Outline each white blood cell.
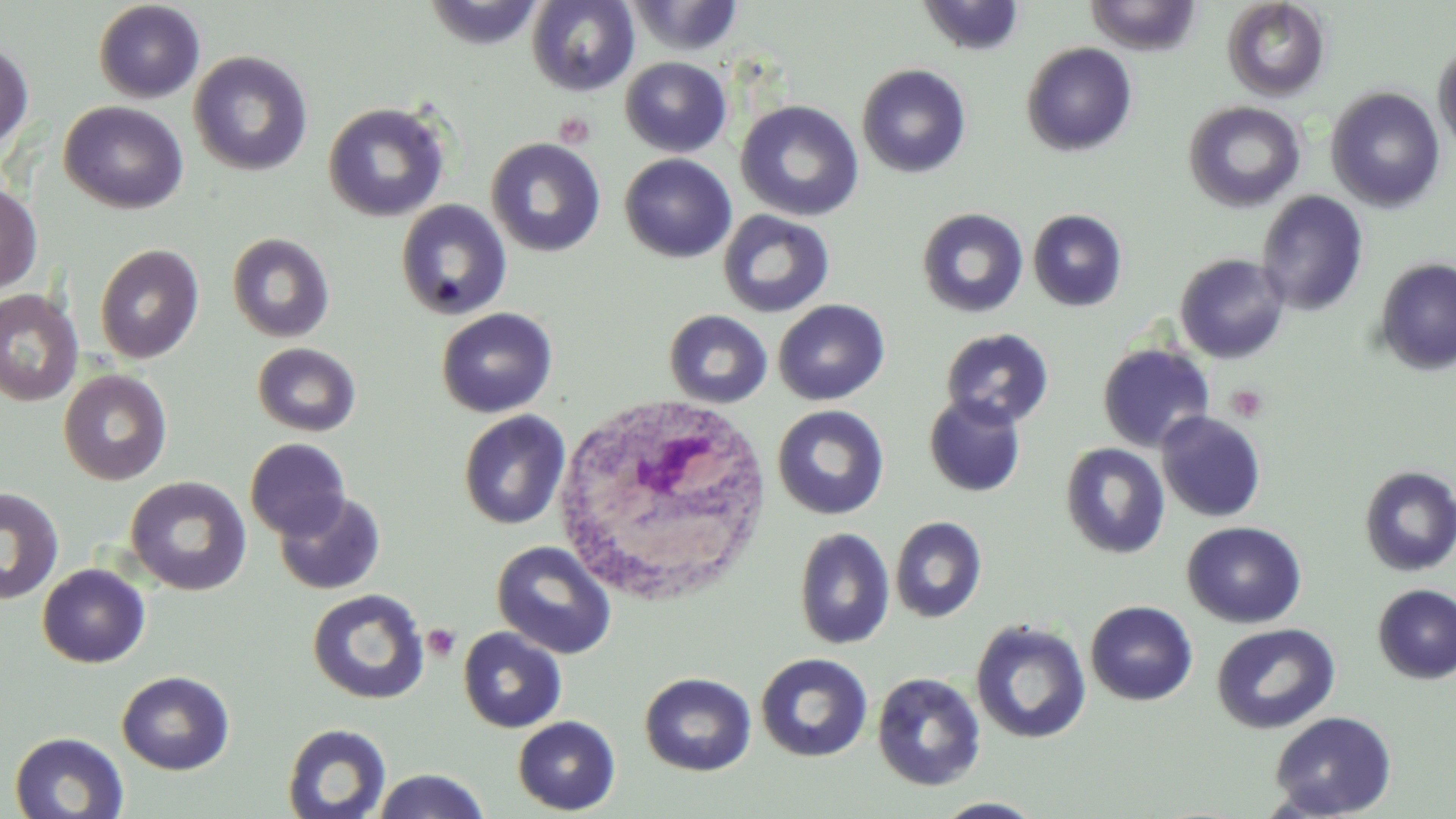

Approximate bounding boxes as named x1/y1/x2/y2 corners in pixels.
White blood cells: (x1=548, y1=393, x2=774, y2=611).

Summary:
  - Uninfected red blood cell locations: (x1=623, y1=0, x2=745, y2=58), (x1=917, y1=0, x2=1027, y2=57), (x1=1084, y1=0, x2=1203, y2=55), (x1=93, y1=1, x2=206, y2=103), (x1=421, y1=1, x2=546, y2=50), (x1=526, y1=1, x2=640, y2=96), (x1=1221, y1=1, x2=1330, y2=102), (x1=0, y1=41, x2=34, y2=151), (x1=1021, y1=42, x2=1138, y2=157), (x1=1433, y1=43, x2=1456, y2=156), (x1=188, y1=51, x2=313, y2=176), (x1=620, y1=56, x2=731, y2=157), (x1=857, y1=63, x2=972, y2=178), (x1=1325, y1=86, x2=1446, y2=212), (x1=58, y1=100, x2=190, y2=214), (x1=736, y1=100, x2=865, y2=221), (x1=1183, y1=100, x2=1305, y2=212), (x1=322, y1=102, x2=451, y2=222), (x1=485, y1=137, x2=606, y2=257), (x1=619, y1=153, x2=737, y2=263), (x1=0, y1=183, x2=43, y2=295), (x1=1256, y1=190, x2=1369, y2=317), (x1=394, y1=199, x2=513, y2=321), (x1=916, y1=207, x2=1029, y2=319), (x1=717, y1=209, x2=835, y2=318), (x1=1027, y1=209, x2=1128, y2=312), (x1=226, y1=232, x2=334, y2=343), (x1=94, y1=243, x2=204, y2=364), (x1=1174, y1=253, x2=1290, y2=364), (x1=1375, y1=258, x2=1456, y2=376), (x1=0, y1=289, x2=83, y2=406), (x1=773, y1=299, x2=890, y2=405), (x1=436, y1=307, x2=558, y2=417), (x1=663, y1=309, x2=772, y2=409), (x1=939, y1=328, x2=1055, y2=429), (x1=252, y1=342, x2=361, y2=437), (x1=1097, y1=343, x2=1214, y2=453), (x1=58, y1=369, x2=173, y2=485), (x1=923, y1=393, x2=1027, y2=497), (x1=772, y1=404, x2=890, y2=520), (x1=458, y1=410, x2=571, y2=530), (x1=1155, y1=411, x2=1267, y2=523), (x1=245, y1=438, x2=351, y2=540), (x1=1060, y1=442, x2=1170, y2=559), (x1=1358, y1=466, x2=1456, y2=577), (x1=124, y1=476, x2=252, y2=596), (x1=0, y1=485, x2=65, y2=605), (x1=273, y1=490, x2=386, y2=595), (x1=889, y1=516, x2=987, y2=623), (x1=1181, y1=521, x2=1307, y2=628), (x1=793, y1=527, x2=895, y2=650), (x1=491, y1=540, x2=617, y2=659), (x1=37, y1=563, x2=151, y2=668), (x1=1372, y1=584, x2=1456, y2=684), (x1=307, y1=588, x2=430, y2=705), (x1=1085, y1=600, x2=1198, y2=706), (x1=970, y1=619, x2=1091, y2=745), (x1=1211, y1=622, x2=1340, y2=735), (x1=457, y1=626, x2=567, y2=733), (x1=755, y1=652, x2=873, y2=762), (x1=116, y1=670, x2=234, y2=775), (x1=639, y1=672, x2=756, y2=776), (x1=871, y1=672, x2=986, y2=792), (x1=1268, y1=710, x2=1397, y2=818), (x1=513, y1=716, x2=620, y2=815), (x1=282, y1=722, x2=392, y2=818), (x1=8, y1=731, x2=129, y2=818), (x1=370, y1=769, x2=492, y2=819), (x1=930, y1=797, x2=1049, y2=818)
  - Platelet locations: (x1=553, y1=113, x2=595, y2=148), (x1=1225, y1=385, x2=1268, y2=422), (x1=421, y1=624, x2=462, y2=661)
  - Slide-level diagnosis: negative for blood parasites
  - Stain: May-Grünwald-Giemsa
  - Preparation: thin blood film
  - Magnification: 1000x
  - Modality: light microscopy
  - Image size: 1456×819 pixels
  - Field of view: one of a larger specimen